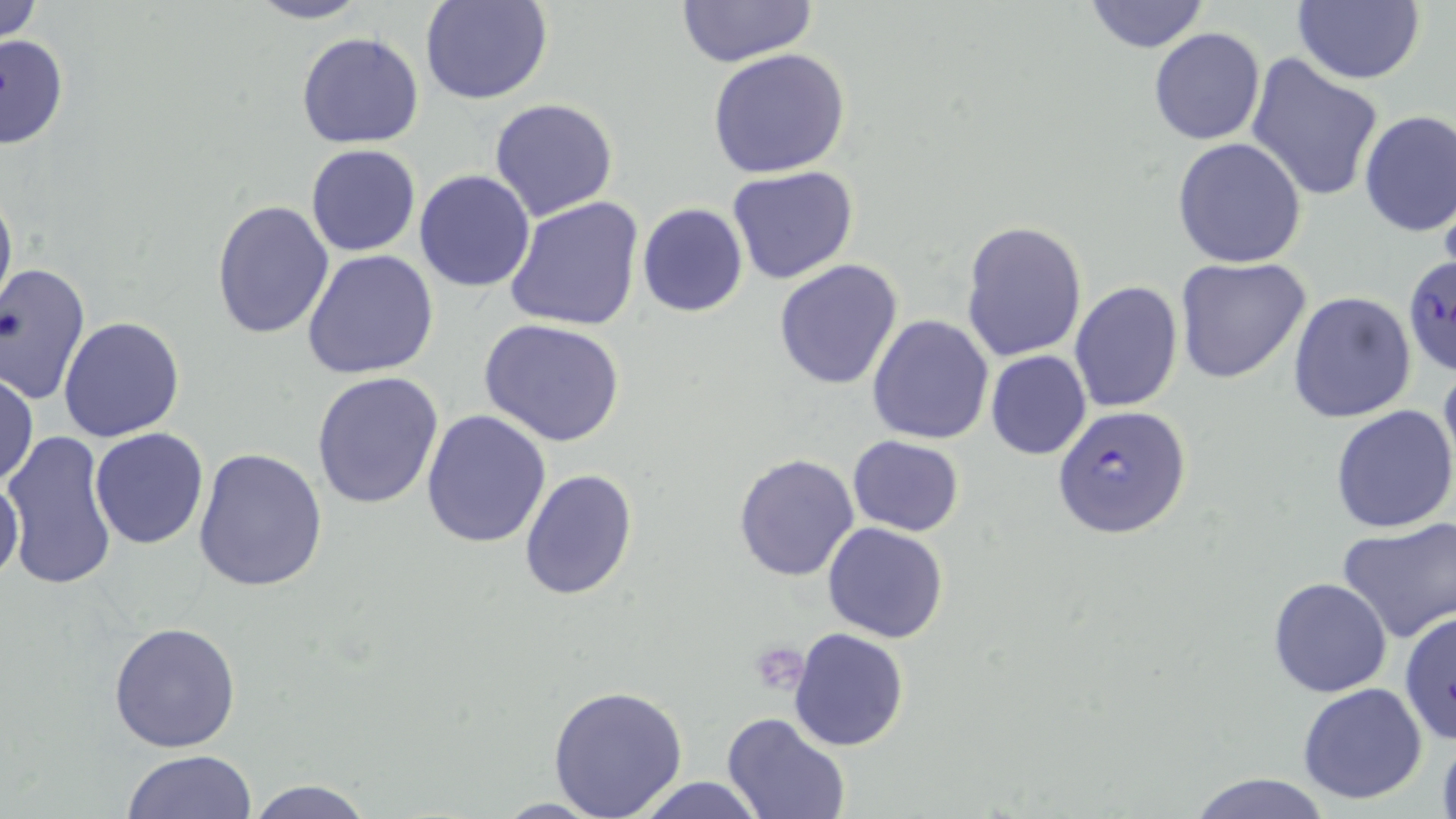

{
  "slide_level_diagnosis": "Plasmodium falciparum",
  "stain": "May-Grünwald-Giemsa",
  "preparation": "thin blood film",
  "platelet_locations": "approximate bounding boxes as (x1, y1, x2, y2) in pixels: (750, 641, 808, 696)",
  "plasmodium_falciparum_infected_red_blood_cell_locations": "approximate bounding boxes as (x1, y1, x2, y2) in pixels: (1402, 252, 1455, 378), (1052, 404, 1192, 540)",
  "magnification": "1000x",
  "uninfected_red_blood_cell_locations": "approximate bounding boxes as (x1, y1, x2, y2) in pixels: (0, 0, 46, 46), (243, 0, 376, 24), (421, 0, 551, 105), (1080, 0, 1213, 53), (1292, 0, 1424, 85), (675, 1, 819, 69), (1149, 28, 1265, 146), (296, 31, 426, 150), (0, 34, 71, 152), (709, 48, 851, 178), (1246, 53, 1384, 203), (489, 98, 619, 222), (1357, 110, 1455, 236), (1172, 138, 1307, 268), (305, 144, 420, 257), (726, 165, 858, 284), (413, 169, 538, 292), (0, 181, 17, 320), (502, 196, 645, 332), (210, 199, 336, 341), (637, 203, 749, 317), (960, 221, 1088, 363), (301, 249, 440, 378), (1175, 258, 1313, 387), (773, 259, 905, 391), (0, 263, 91, 404), (1068, 279, 1182, 413), (1288, 291, 1416, 425), (867, 313, 995, 445), (58, 316, 186, 443), (479, 318, 627, 447), (985, 350, 1092, 460), (1438, 354, 1456, 486), (1, 370, 38, 490), (311, 371, 444, 510), (1330, 406, 1456, 533), (421, 408, 552, 548), (91, 427, 209, 549), (4, 429, 120, 593), (847, 435, 965, 536), (193, 448, 328, 595), (732, 452, 860, 580), (519, 467, 638, 598), (0, 473, 26, 589), (1337, 517, 1455, 643), (823, 523, 949, 644), (1267, 576, 1393, 698), (1398, 608, 1455, 744), (108, 622, 242, 752), (788, 628, 910, 751), (1297, 682, 1429, 805), (547, 683, 689, 818), (723, 713, 850, 819), (1437, 730, 1456, 819), (119, 749, 258, 819), (1186, 772, 1333, 818), (629, 776, 769, 818), (244, 777, 378, 819)",
  "field_of_view": "single",
  "image_size": "1456×819 pixels",
  "modality": "light microscopy"
}